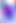

magnification = 400x
identification = Toxoplasma gondii
modality = photomicrograph